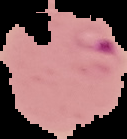 Malaria status: parasitized. Image is 127×139 pixels. Cell region segmented out of the field of view; the surrounding area is masked to black. From a thin blood smear.